Give the extent of all Plasmodium falciparum-infected red blood cells.
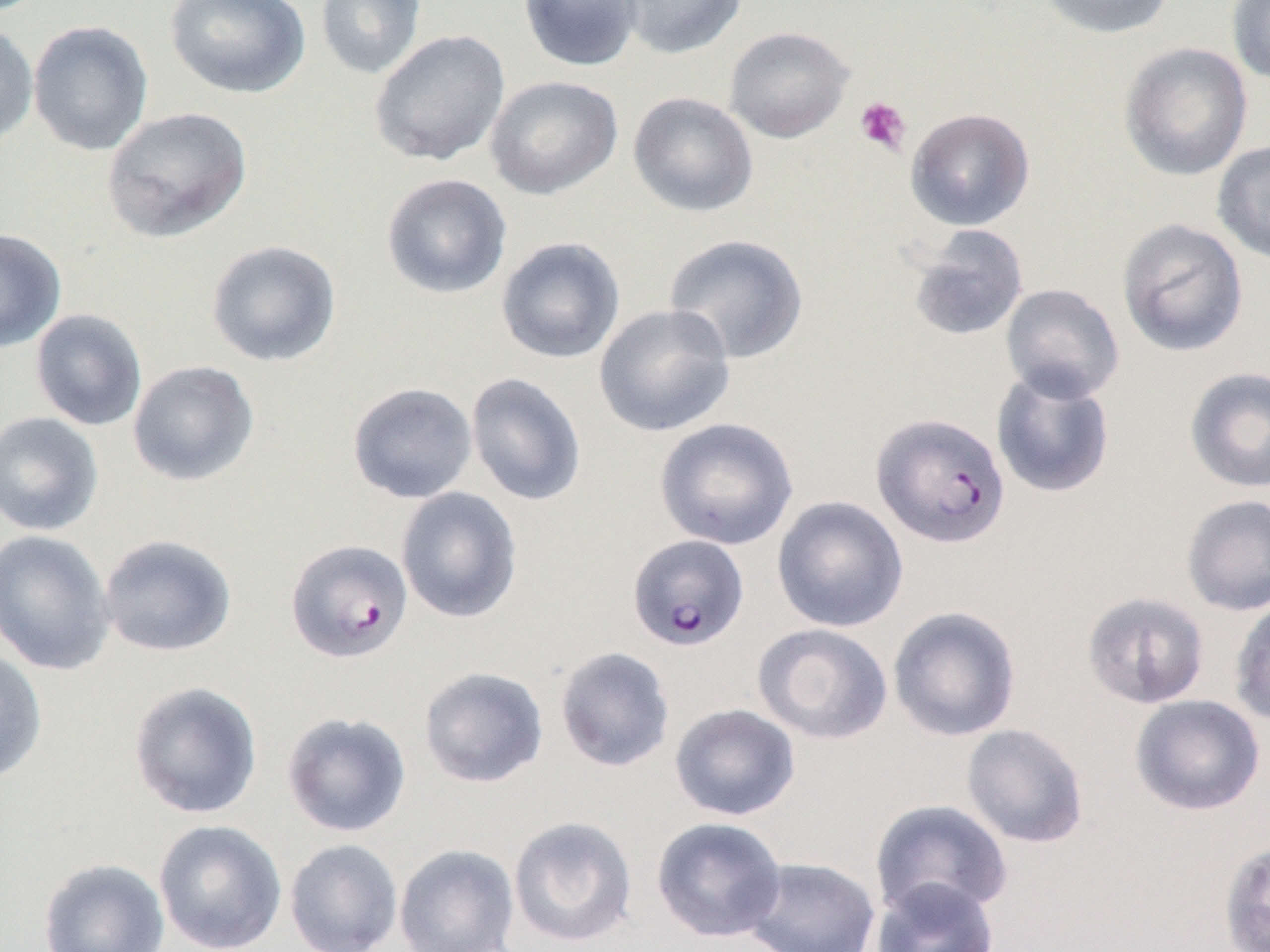

Approximate bounding boxes as named x1/y1/x2/y2 corners in pixels.
Plasmodium falciparum-infected red blood cells: (x1=871, y1=411, x2=1011, y2=549), (x1=627, y1=534, x2=749, y2=651), (x1=285, y1=538, x2=413, y2=663).

Uninfected red blood cell locations: (x1=164, y1=0, x2=311, y2=99), (x1=314, y1=0, x2=427, y2=80), (x1=518, y1=0, x2=643, y2=72), (x1=616, y1=0, x2=748, y2=59), (x1=1037, y1=0, x2=1175, y2=39), (x1=1226, y1=0, x2=1270, y2=85), (x1=28, y1=19, x2=154, y2=156), (x1=0, y1=21, x2=39, y2=147), (x1=724, y1=26, x2=855, y2=143), (x1=369, y1=28, x2=511, y2=168), (x1=1118, y1=41, x2=1253, y2=181), (x1=484, y1=75, x2=623, y2=200), (x1=628, y1=91, x2=759, y2=218), (x1=101, y1=106, x2=252, y2=243), (x1=905, y1=107, x2=1035, y2=231), (x1=1212, y1=140, x2=1270, y2=265), (x1=380, y1=173, x2=513, y2=299), (x1=1117, y1=218, x2=1249, y2=357), (x1=905, y1=224, x2=1030, y2=342), (x1=0, y1=228, x2=66, y2=352), (x1=663, y1=233, x2=809, y2=365), (x1=495, y1=237, x2=626, y2=364), (x1=206, y1=239, x2=342, y2=367), (x1=1000, y1=283, x2=1125, y2=403), (x1=593, y1=303, x2=736, y2=437), (x1=30, y1=308, x2=148, y2=431), (x1=127, y1=360, x2=260, y2=486), (x1=1184, y1=366, x2=1270, y2=494), (x1=990, y1=368, x2=1116, y2=499), (x1=465, y1=372, x2=588, y2=507), (x1=346, y1=381, x2=478, y2=504), (x1=0, y1=411, x2=104, y2=536), (x1=654, y1=417, x2=799, y2=551), (x1=395, y1=486, x2=523, y2=624), (x1=1181, y1=493, x2=1270, y2=616), (x1=772, y1=495, x2=909, y2=633), (x1=0, y1=529, x2=115, y2=675), (x1=98, y1=534, x2=237, y2=658), (x1=1081, y1=591, x2=1210, y2=709), (x1=1229, y1=596, x2=1270, y2=727), (x1=887, y1=605, x2=1022, y2=742), (x1=751, y1=623, x2=893, y2=745), (x1=0, y1=646, x2=48, y2=784), (x1=555, y1=646, x2=675, y2=772), (x1=417, y1=666, x2=549, y2=788), (x1=127, y1=681, x2=263, y2=819), (x1=1129, y1=694, x2=1266, y2=816), (x1=669, y1=703, x2=801, y2=821), (x1=281, y1=711, x2=412, y2=838), (x1=961, y1=723, x2=1089, y2=848), (x1=869, y1=799, x2=1013, y2=921), (x1=508, y1=815, x2=638, y2=948), (x1=651, y1=816, x2=787, y2=942), (x1=153, y1=819, x2=287, y2=952), (x1=284, y1=838, x2=404, y2=951), (x1=1218, y1=838, x2=1270, y2=952), (x1=393, y1=843, x2=520, y2=952), (x1=741, y1=856, x2=881, y2=952), (x1=38, y1=857, x2=170, y2=952), (x1=870, y1=877, x2=1000, y2=952). Platelet locations: (x1=854, y1=96, x2=912, y2=156). Slide-level diagnosis: Plasmodium falciparum. Single field of view. Image is 1270×952 pixels. Light microscopy. 1000x magnification. Thin blood smear.